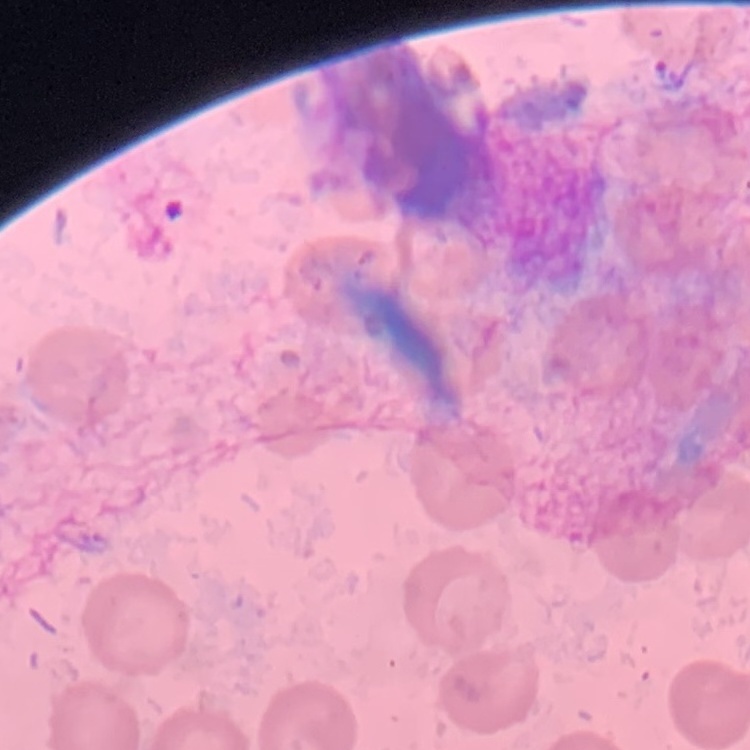
The red blood cells show no rouleaux formation. Thin blood film. One tile cut from a larger photomicrograph. Stained with either Field's or Giemsa.